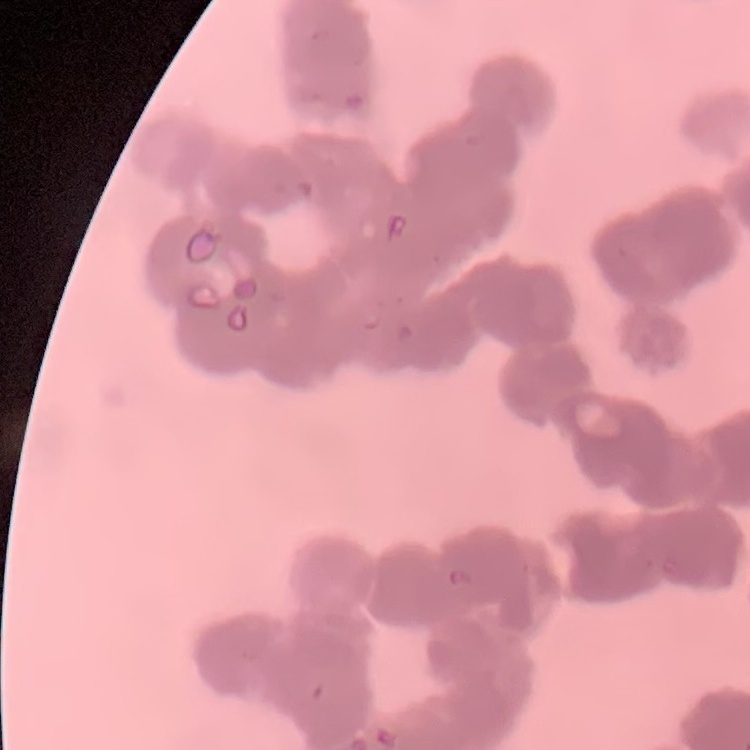

The red blood cells exhibit rouleaux formation. Stained with either Field's or Giemsa. Square crop of a larger photomicrograph. Thin blood smear.